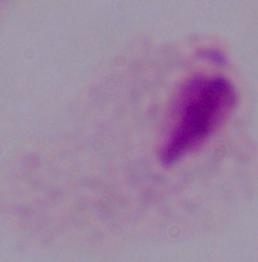

{
  "modality": "micrograph",
  "identification": "trichomonad",
  "magnification": "1000x"
}